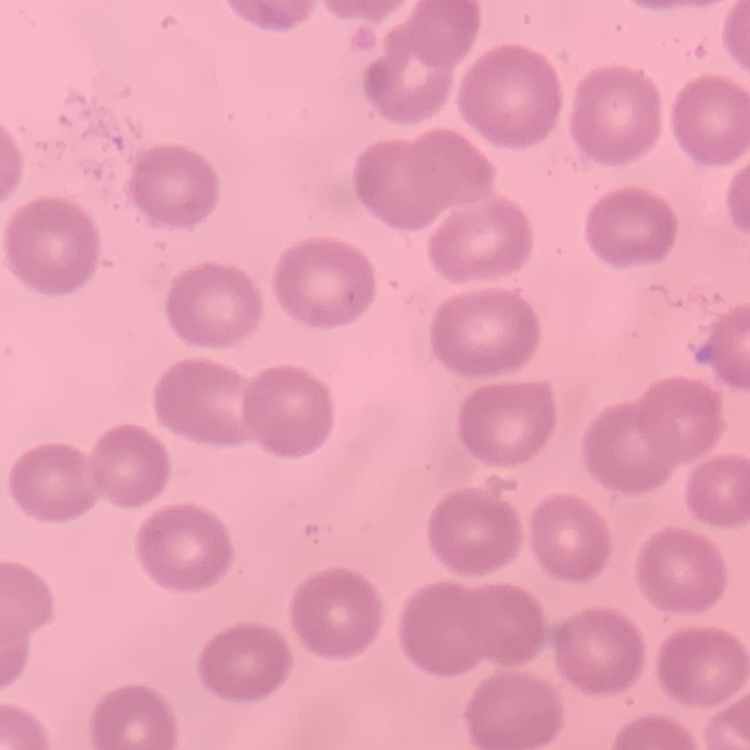

Summary:
  - Erythrocyte morphology: no rouleaux formation
  - Stain: Field's or Giemsa
  - Image type: one tile cut from a larger photomicrograph
  - Preparation: thin peripheral smear